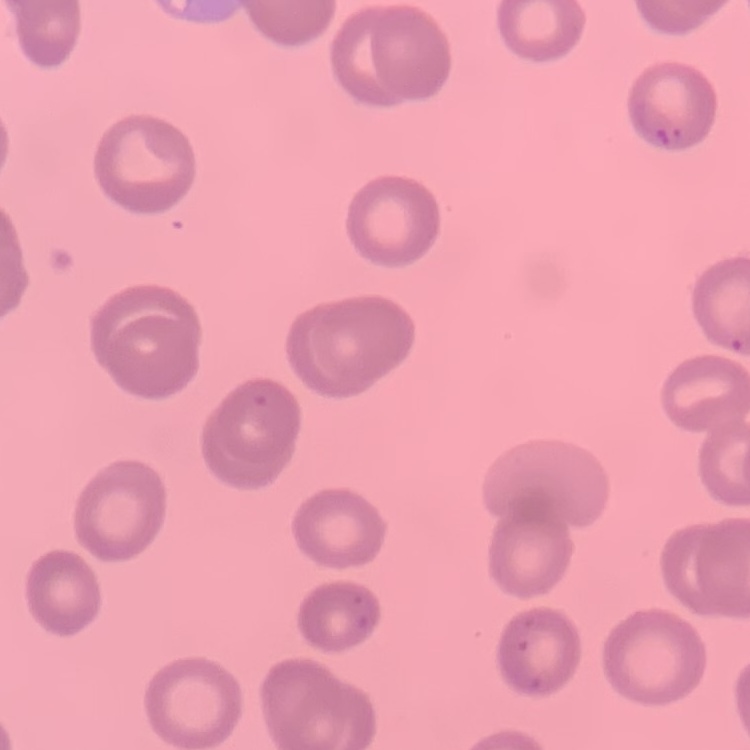
Summary:
  - Erythrocyte morphology: no rouleaux formation
  - Stain: Field's or Giemsa
  - Preparation: thin peripheral smear
  - Image type: one tile cut from a larger photomicrograph